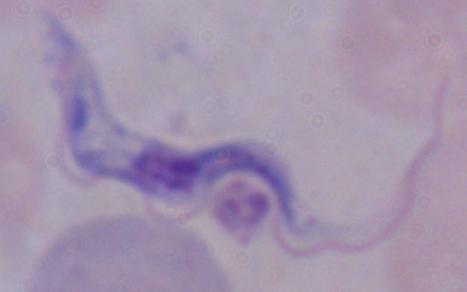

identification = trypanosome
magnification = 1000x
modality = photomicrograph